Identify the cell.
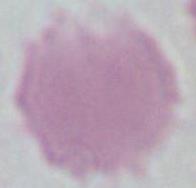
An erythrocyte.

Summary:
  - Magnification: 1000x
  - Modality: micrograph